Report the malaria status of this cell.
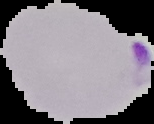
Parasitized.

Cell region segmented out of the field of view; the surrounding area is masked to black. Image is 154×124 pixels. From a thin blood smear.